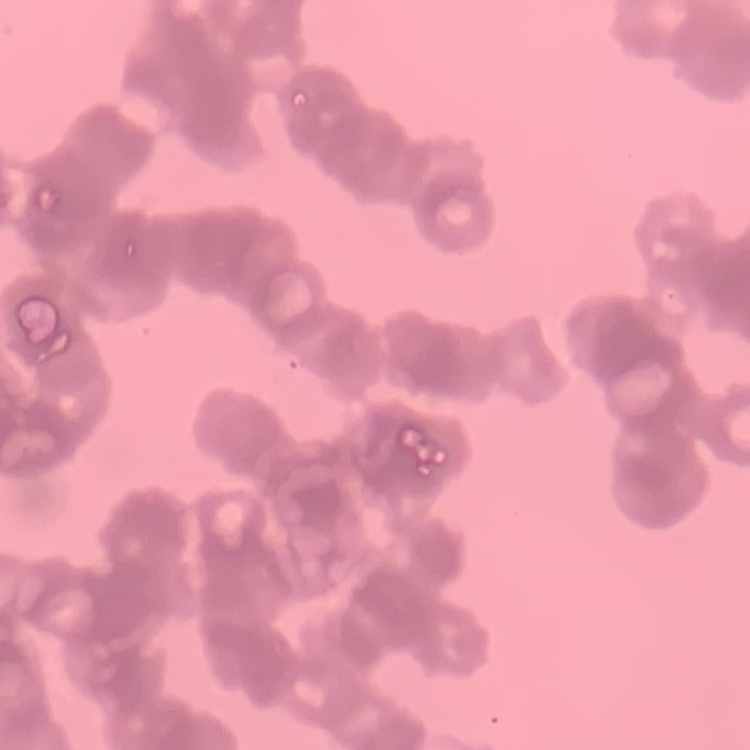

{
  "red_blood_cell_morphology": "rouleaux formation",
  "stain": "Field's or Giemsa",
  "preparation": "thin blood smear",
  "image_type": "square crop of a larger photomicrograph"
}